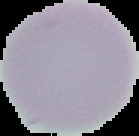

image size = 139×136 pixels
malaria status = uninfected
preparation = thin blood film
image type = cell region segmented out of the field of view; surrounding area masked to black